Identify the parasite.
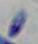

This is Toxoplasma gondii.

Summary:
  - Modality: micrograph
  - Magnification: 1000x